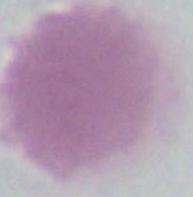

identification = erythrocyte
magnification = 1000x
modality = photomicrograph